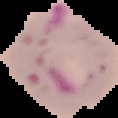 Image is 118×118 pixels. From a thin blood smear. Cell region segmented out of the field of view; the surrounding area is masked to black. Result: Plasmodium parasites identified.